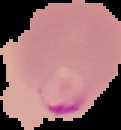
image type = segmented cell region on a black background
malaria status = parasitized
preparation = thin blood smear
image size = 121×130 pixels